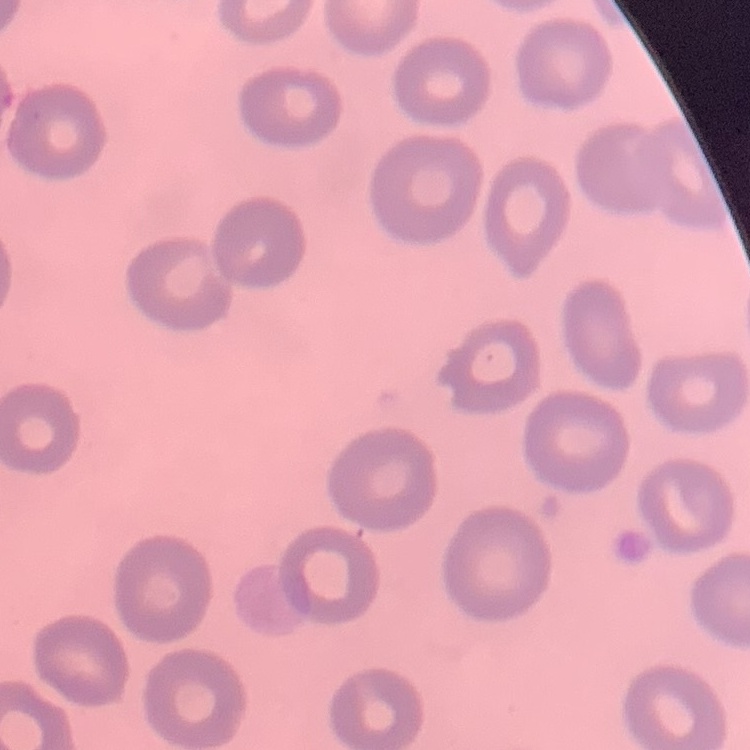

red blood cell morphology = no rouleaux formation
stain = Field's or Giemsa
image type = square crop of a larger photomicrograph
preparation = thin blood film